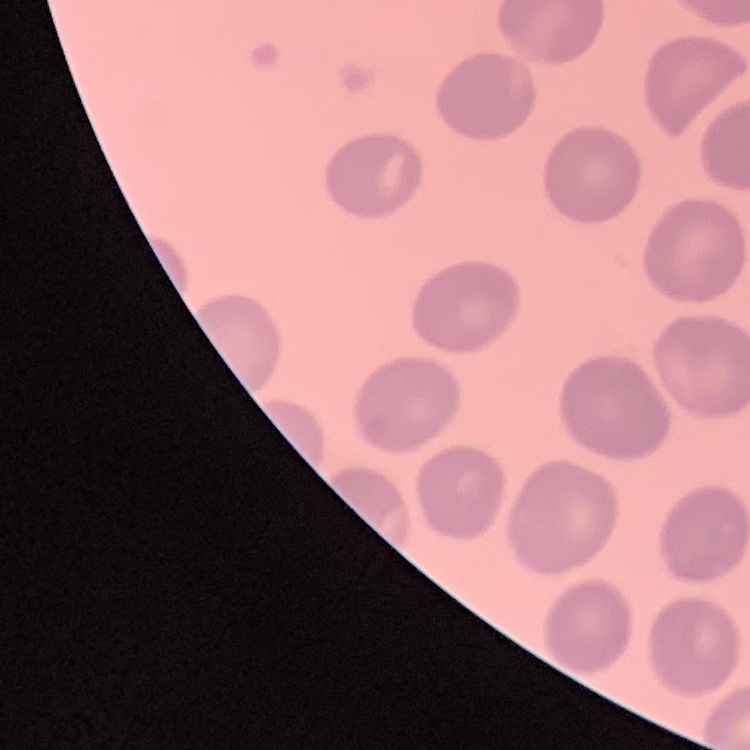

{
  "red_blood_cell_morphology": "no rouleaux formation",
  "stain": "Field's or Giemsa",
  "preparation": "thin blood smear",
  "image_type": "square crop of a larger photomicrograph"
}